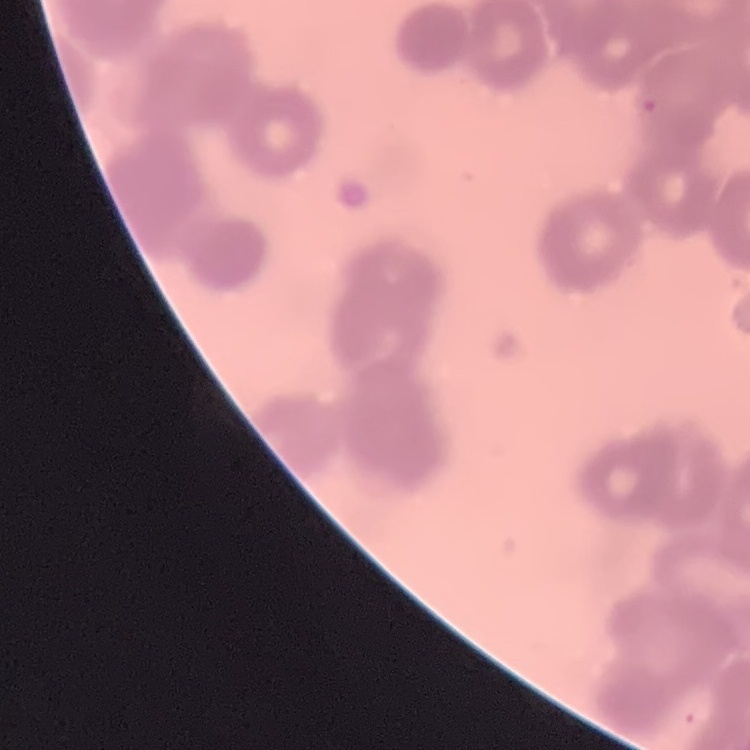
The erythrocytes show rouleaux formation. One tile cut from a larger photomicrograph. Field's or Giemsa stain. Thin blood film.